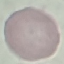
Result: no malaria parasites detected. Giemsa-stained preparation. Thin blood film. Cell patch, automatically extracted from a larger field of view and resized to 64 × 64 pixels. Acquired by smartphone through the microscope eyepiece.